State which cell type is depicted.
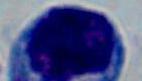
A leukocyte.

Photomicrograph. 1000x magnification.